Assess the morphology of the red blood cells.
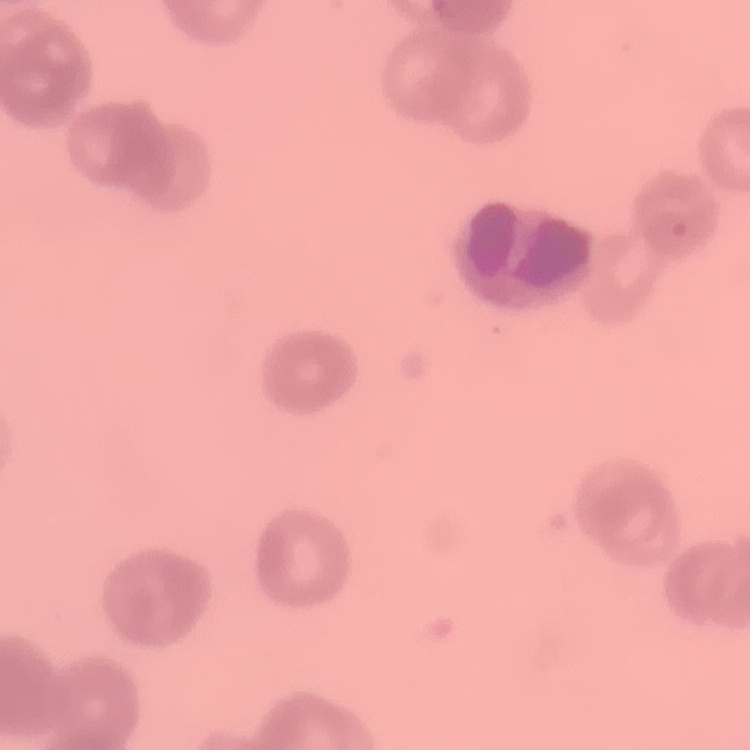
Rouleaux formation.

Square crop of a larger photomicrograph. Thin blood smear. Stained with either Field's or Giemsa.